Assess this cell for malaria.
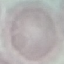
Uninfected.

Thin blood film. Photographed with a smartphone camera at the microscope eyepiece. Giemsa stain. Cell patch, automatically extracted from a larger field of view and resized to 64 × 64 pixels.